Identify the parasite.
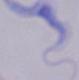
A trypanosome.

1000x magnification. Photomicrograph.